Identify the cell.
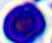
A leukocyte.

Summary:
  - Magnification: 400x
  - Modality: photomicrograph